Classify this cell by malaria status.
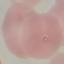
Parasitized.

Thin smear of blood. Acquired by smartphone through the microscope eyepiece. Giemsa-stained preparation. Cell patch, automatically extracted from a larger field of view and resized to 64 × 64 pixels.